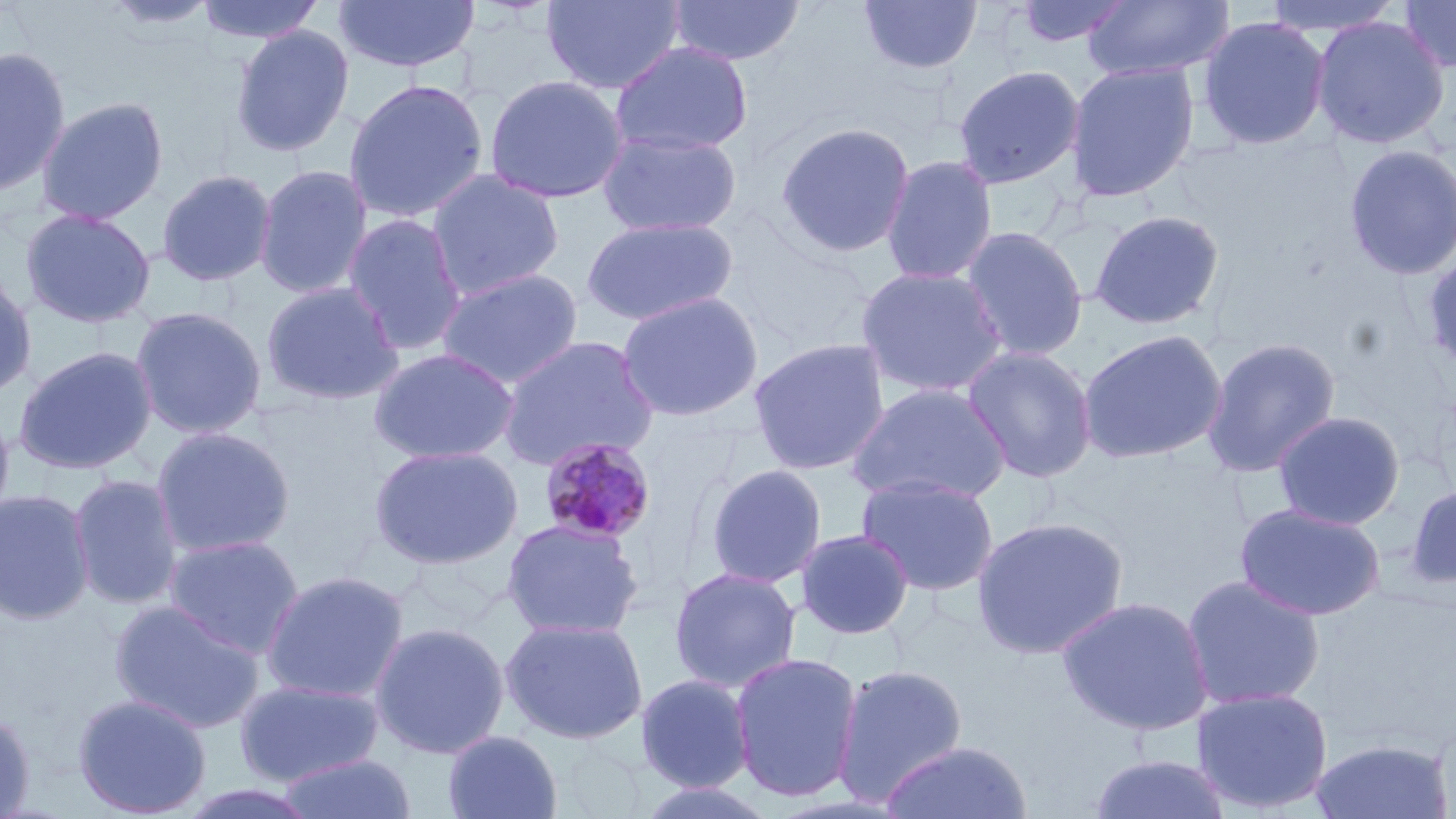

Summary:
  - Coordinate format: approximate bounding boxes as [x1, y1, x2, y2] in pixels
  - Plasmodium malariae-infected red blood cell locations: [537, 436, 658, 546]
  - Uninfected red blood cell locations: [195, 0, 326, 45], [334, 0, 479, 73], [542, 0, 686, 95], [666, 0, 805, 66], [857, 0, 983, 77], [1013, 0, 1131, 48], [1259, 0, 1406, 38], [1397, 0, 1456, 73], [101, 1, 221, 33], [1083, 1, 1234, 82], [1197, 15, 1330, 150], [1310, 15, 1451, 150], [230, 24, 355, 157], [611, 41, 754, 156], [0, 45, 71, 197], [1064, 61, 1200, 202], [952, 64, 1086, 190], [483, 74, 630, 204], [343, 78, 489, 224], [36, 96, 169, 225], [774, 121, 915, 259], [596, 129, 743, 238], [1342, 143, 1456, 281], [881, 155, 998, 285], [254, 164, 373, 299], [156, 168, 277, 287], [426, 169, 565, 301], [20, 207, 156, 328], [1089, 209, 1225, 330], [341, 213, 468, 356], [581, 216, 739, 327], [959, 225, 1089, 362], [1421, 248, 1456, 375], [854, 265, 1009, 398], [0, 267, 38, 401], [436, 267, 585, 389], [260, 279, 405, 406], [616, 291, 764, 422], [130, 305, 268, 440], [1077, 329, 1228, 465], [497, 335, 660, 471], [1201, 336, 1342, 478], [747, 337, 891, 476], [13, 345, 158, 475], [962, 345, 1098, 483], [368, 347, 520, 464], [845, 382, 1012, 505], [0, 403, 16, 533], [1273, 410, 1405, 530], [151, 425, 296, 558], [368, 444, 523, 570], [703, 463, 828, 589], [856, 472, 1000, 596], [68, 473, 183, 611], [1403, 482, 1456, 591], [0, 489, 94, 625], [1234, 502, 1386, 621], [971, 515, 1129, 659], [501, 518, 645, 641], [794, 528, 915, 640], [164, 534, 305, 658], [668, 566, 802, 693], [259, 570, 410, 704], [1181, 574, 1326, 711], [1056, 595, 1215, 736], [109, 599, 266, 734], [500, 617, 649, 745], [369, 621, 510, 759], [729, 651, 863, 802], [832, 663, 969, 806], [635, 673, 755, 792], [233, 677, 385, 788], [1191, 686, 1334, 814], [72, 693, 212, 818], [0, 709, 36, 817], [442, 729, 563, 819], [1307, 738, 1453, 818], [879, 740, 1032, 819], [278, 752, 418, 819], [1087, 753, 1233, 819], [632, 779, 781, 819], [173, 781, 325, 819]
  - Slide-level diagnosis: Plasmodium malariae
  - Magnification: 1000x
  - Image size: 1456×819 pixels
  - Stain: May-Grünwald-Giemsa
  - Field of view: single
  - Preparation: thin blood film
  - Modality: light microscopy